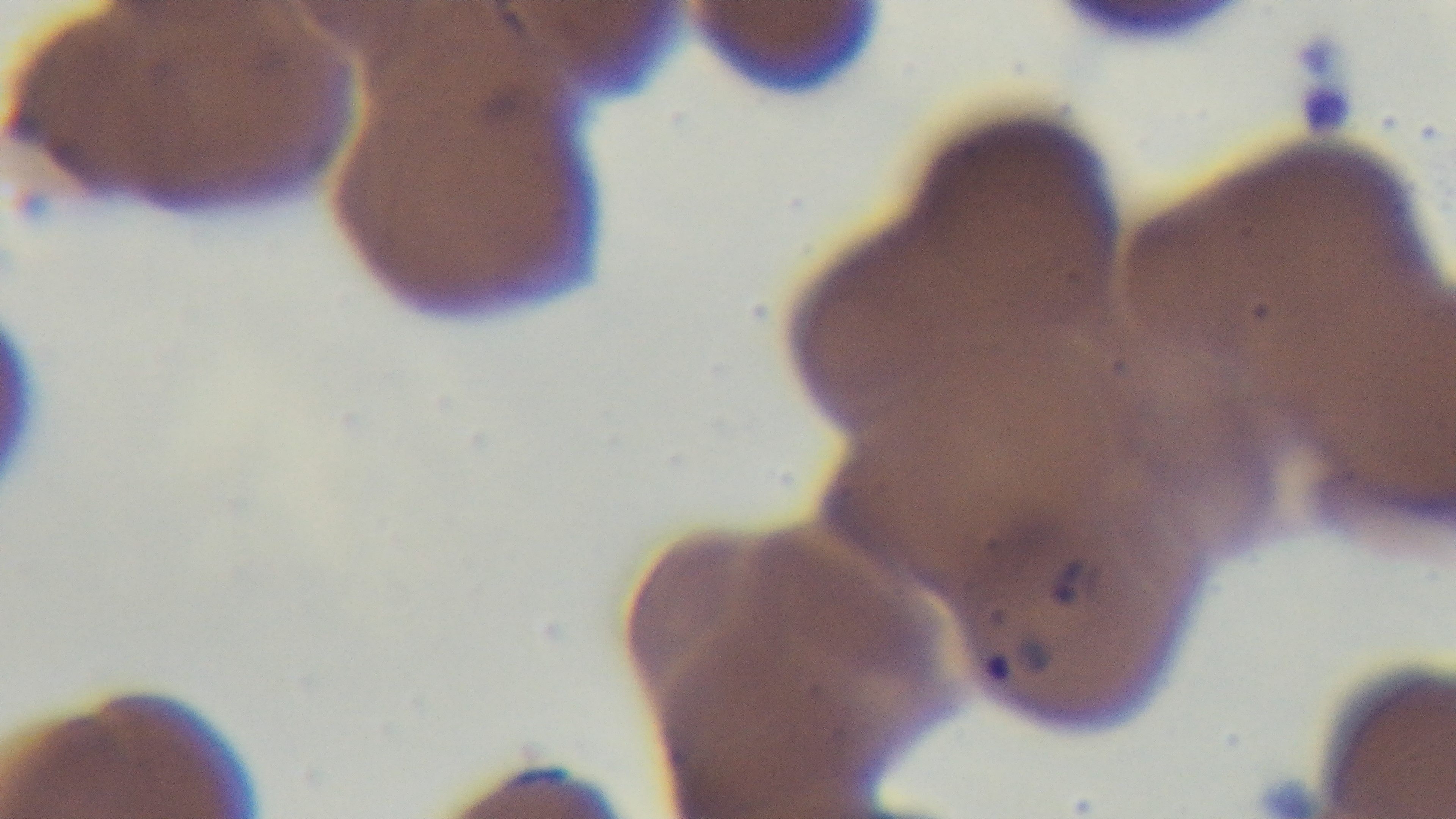

capture: mounted 4K digital camera
modality: light microscopy
malaria_status: positive
preparation: thin
field_of_view: single
stain: Giemsa
objective: 100x oil immersion